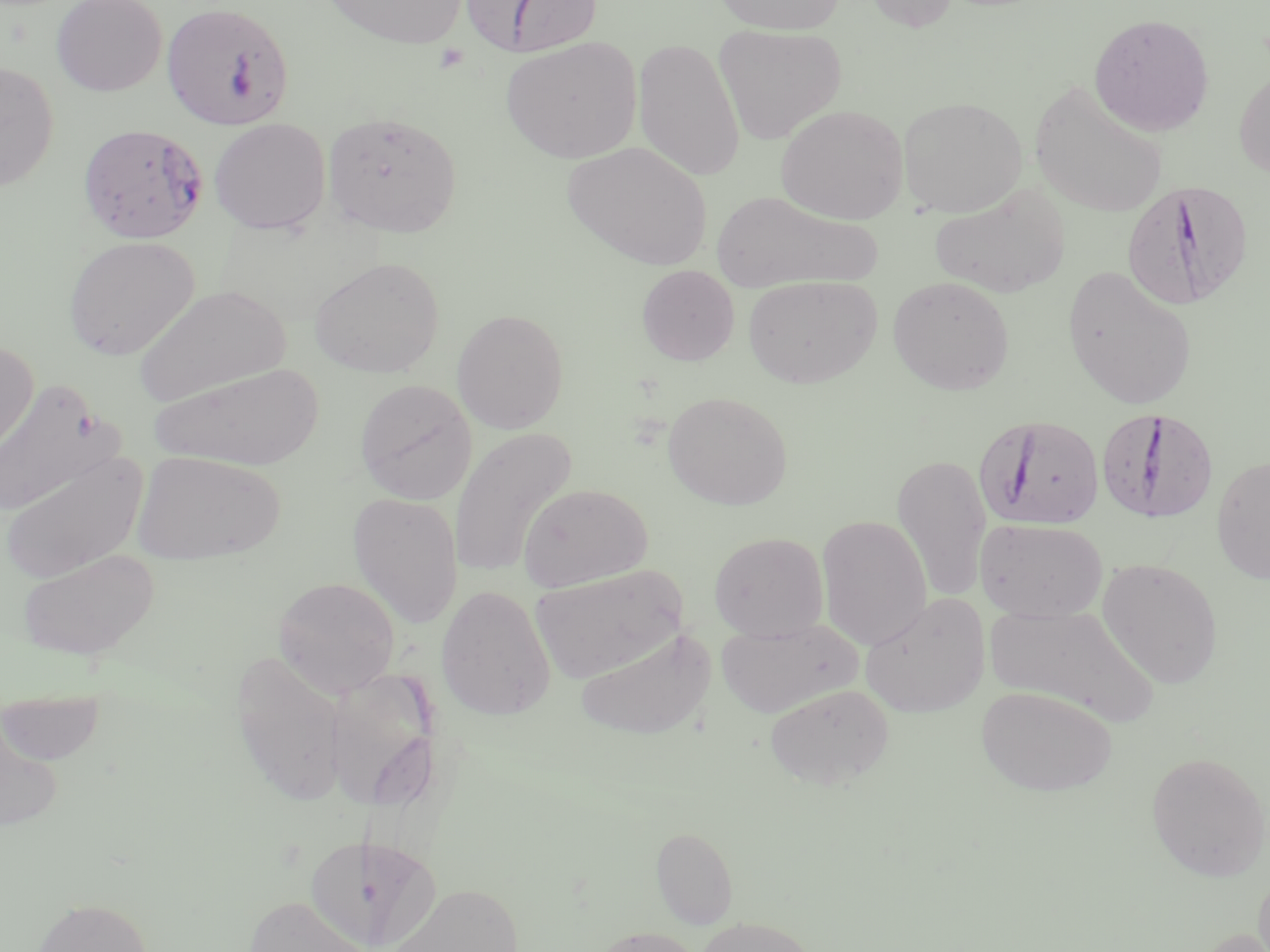
Summary:
  - Coordinate format: approximate bounding boxes as (x1,y1)-(x2,y2) corner pairs in pixels
  - Uninfected red blood cell locations: (50,0)-(167,96), (320,0)-(468,49), (712,0)-(846,35), (861,0)-(961,32), (1089,13)-(1215,137), (714,25)-(847,145), (501,36)-(643,163), (633,37)-(745,182), (0,61)-(59,191), (1234,65)-(1270,179), (1030,82)-(1168,218), (897,96)-(1027,217), (776,104)-(909,224), (322,111)-(462,237), (209,118)-(331,234), (563,142)-(711,269), (928,184)-(1069,298), (710,190)-(879,293), (63,235)-(199,361), (309,256)-(445,378), (636,264)-(739,366), (1062,265)-(1198,410), (742,275)-(882,388), (887,276)-(1015,396), (133,284)-(291,407), (451,308)-(569,433), (0,340)-(38,460), (150,363)-(324,470), (355,378)-(477,504), (0,380)-(114,519), (663,391)-(793,510), (449,427)-(577,578), (1,449)-(147,584), (132,451)-(285,565), (891,452)-(993,603), (1211,455)-(1270,585), (518,484)-(653,592), (347,491)-(464,630), (816,514)-(933,650), (976,518)-(1108,622), (709,532)-(829,641), (17,548)-(160,660), (1097,558)-(1224,688), (530,564)-(689,683), (274,576)-(401,697), (435,585)-(556,721), (860,592)-(991,717), (986,602)-(1158,726), (714,618)-(861,719), (575,627)-(716,741), (230,651)-(349,805), (321,667)-(443,811), (764,683)-(894,790), (976,686)-(1116,795), (1,687)-(107,766), (0,711)-(64,834), (1146,751)-(1269,882), (651,826)-(738,928), (304,836)-(399,952), (1254,868)-(1270,952), (385,883)-(524,952), (243,895)-(372,952), (31,897)-(153,952), (696,917)-(817,952), (589,926)-(706,952)
  - Plasmodium falciparum-infected red blood cell locations: (462,0)-(604,58), (161,1)-(295,132), (77,122)-(209,244), (1122,179)-(1255,309), (1095,406)-(1219,525), (975,414)-(1106,530)
  - Platelet locations: (433,44)-(471,74)
  - Slide-level diagnosis: Plasmodium falciparum
  - Field of view: one of a larger specimen
  - Modality: light microscopy
  - Preparation: thin blood smear
  - Image size: 1270×952 pixels
  - Stain: May-Grünwald-Giemsa
  - Magnification: 1000x